Give the extent of all uninfected red blood cells.
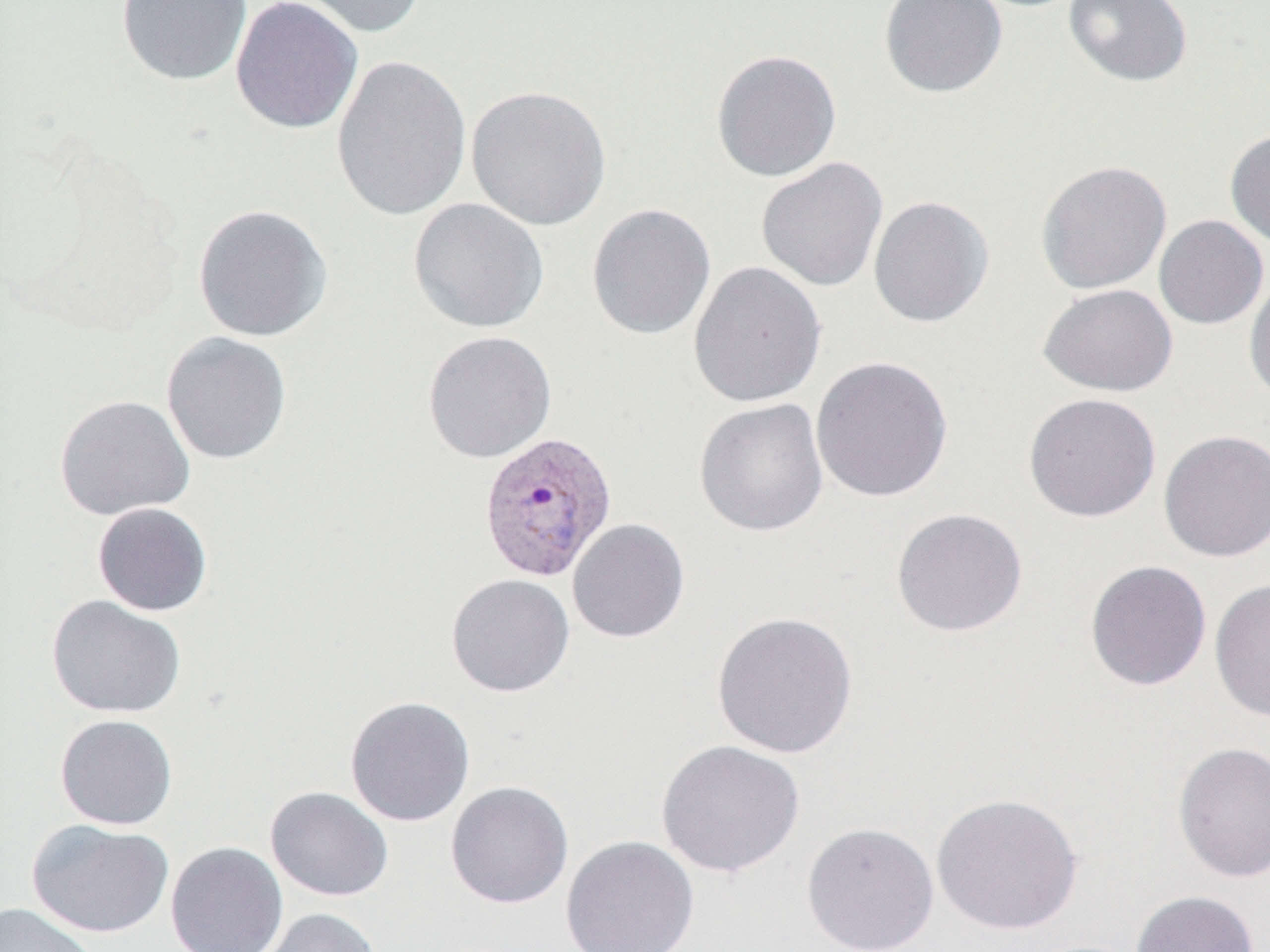

Approximate bounding boxes as (x1,y1)-(x2,y2) corner pairs in pixels.
Uninfected red blood cells: (115,0)-(253,86), (230,0)-(363,134), (286,0)-(429,38), (878,0)-(1008,99), (1063,0)-(1193,87), (710,49)-(842,183), (330,53)-(472,222), (465,84)-(611,231), (1224,128)-(1270,249), (756,157)-(888,292), (1035,159)-(1173,294), (868,195)-(995,329), (408,197)-(550,333), (192,203)-(333,343), (586,203)-(716,341), (1154,215)-(1268,330), (688,261)-(827,409), (1244,271)-(1270,407), (1036,283)-(1178,397), (422,330)-(557,464), (161,332)-(293,465), (810,355)-(954,503), (1023,392)-(1161,523), (54,394)-(195,520), (694,398)-(829,537), (1158,429)-(1270,562), (92,502)-(213,617), (890,507)-(1028,637), (567,518)-(690,643), (1084,560)-(1212,691), (445,573)-(575,697), (1209,579)-(1270,721), (46,595)-(186,718), (711,611)-(859,759), (344,695)-(476,827), (54,714)-(178,830), (656,739)-(806,878), (1172,741)-(1270,884), (445,781)-(574,909), (265,786)-(393,902), (930,792)-(1084,935), (26,818)-(174,938), (801,821)-(939,952), (560,835)-(700,952), (165,841)-(289,952), (1129,890)-(1260,952), (0,901)-(99,951), (251,907)-(383,952).

Summary:
  - Plasmodium vivax-infected red blood cell locations: (477,432)-(617,582)
  - Slide-level diagnosis: Plasmodium vivax
  - Image size: 1270×952 pixels
  - Modality: light microscopy
  - Stain: May-Grünwald-Giemsa
  - Preparation: thin blood film
  - Magnification: 1000x
  - Field of view: one of a larger specimen